Classify this cell by malaria status.
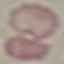
Uninfected.

capture = smartphone through the microscope eyepiece
stain = Giemsa
preparation = thin smear
image type = automatically extracted cell patch, resized to 64 × 64 pixels